State which parasite is depicted.
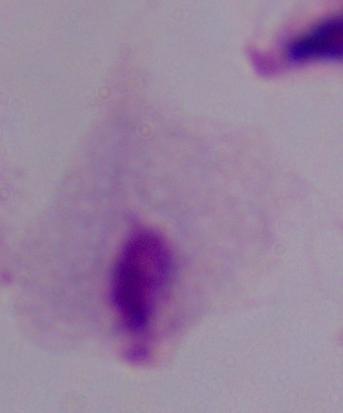

This is a trichomonad.

Micrograph. 1000x magnification.